Assess this cell for malaria.
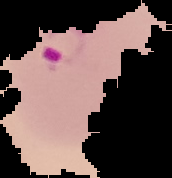
It is parasitized.

Summary:
  - Image size: 172×178 pixels
  - Preparation: thin blood film
  - Image type: cell region segmented out of the field of view; surrounding area masked to black